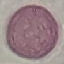
Summary:
  - Result: no malaria parasites detected
  - Image type: cell patch, automatically extracted from a larger field of view and resized to 64 × 64 pixels
  - Stain: Giemsa
  - Capture: smartphone through the microscope eyepiece
  - Preparation: thin smear